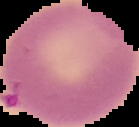

Summary:
  - Malaria status: uninfected
  - Image size: 139×127 pixels
  - Image type: cell region segmented out of the field of view; surrounding area masked to black
  - Preparation: thin blood film